State which parasite is depicted.
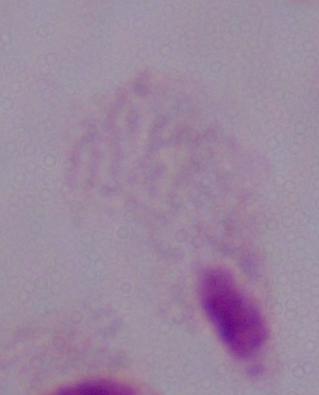
A trichomonad.

1000x magnification. Micrograph.